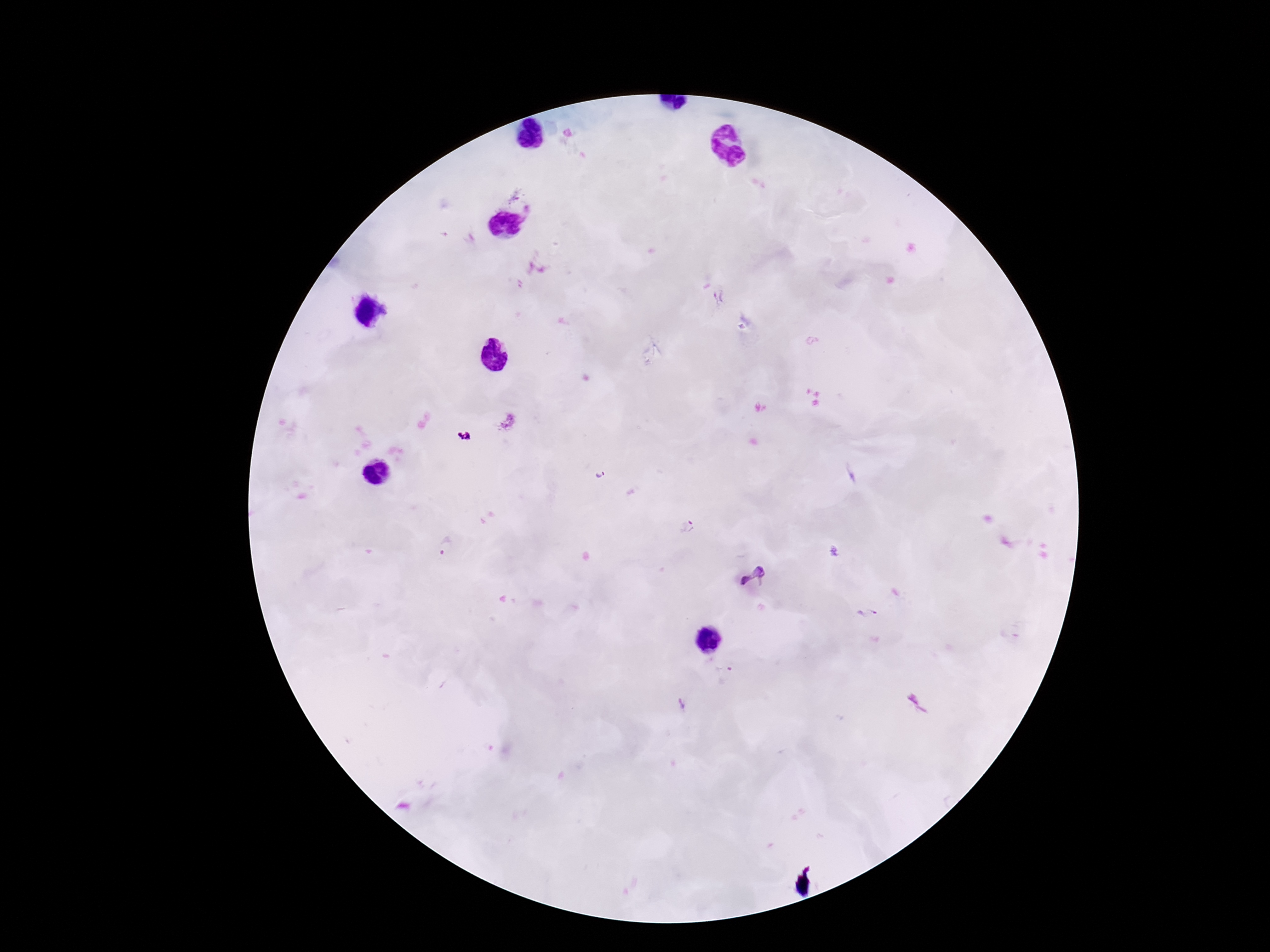
preparation = thick peripheral-blood smear
capture = smartphone camera through the microscope eyepiece
image size = 1270×952 pixels
patient malaria status = positive
Plasmodium parasite locations = approximate centers as [x, y] in pixels: [512, 196], [530, 211], [718, 298], [506, 422], [600, 473], [688, 526], [444, 547], [756, 577], [867, 614], [725, 675], [681, 704]
field of view = single
stain = Giemsa
magnification = 100x